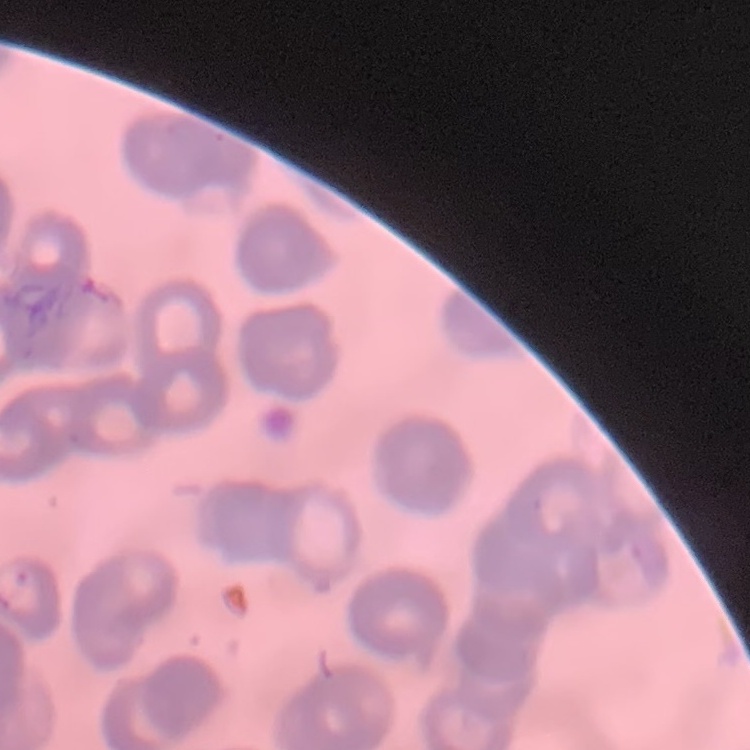
Summary:
  - Red blood cell morphology: rouleaux formation
  - Stain: Field's or Giemsa
  - Preparation: thin blood smear
  - Image type: square crop of a larger photomicrograph